Comment on the morphology of the erythrocytes.
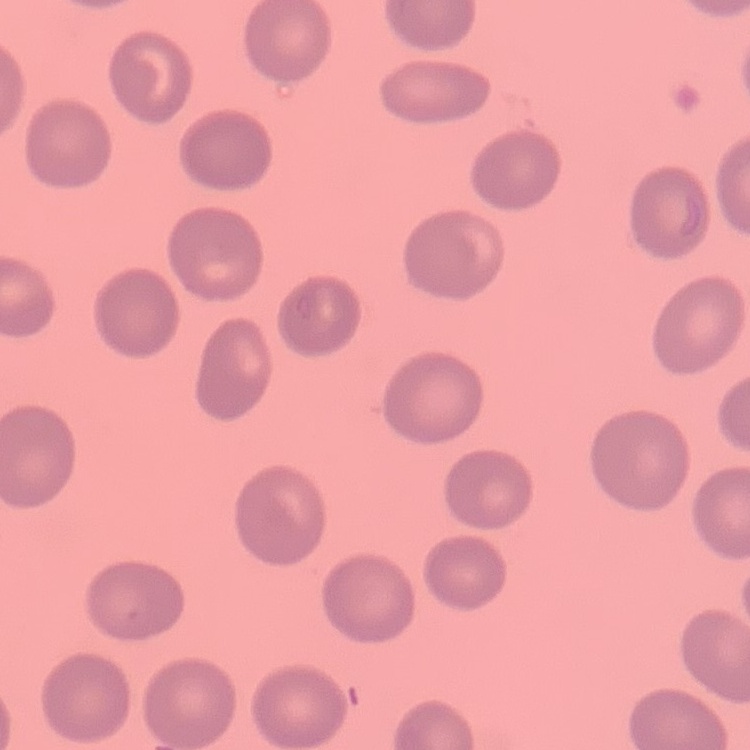
They show no rouleaux formation.

Summary:
  - Stain: Field's or Giemsa
  - Image type: square crop of a larger photomicrograph
  - Preparation: thin blood smear